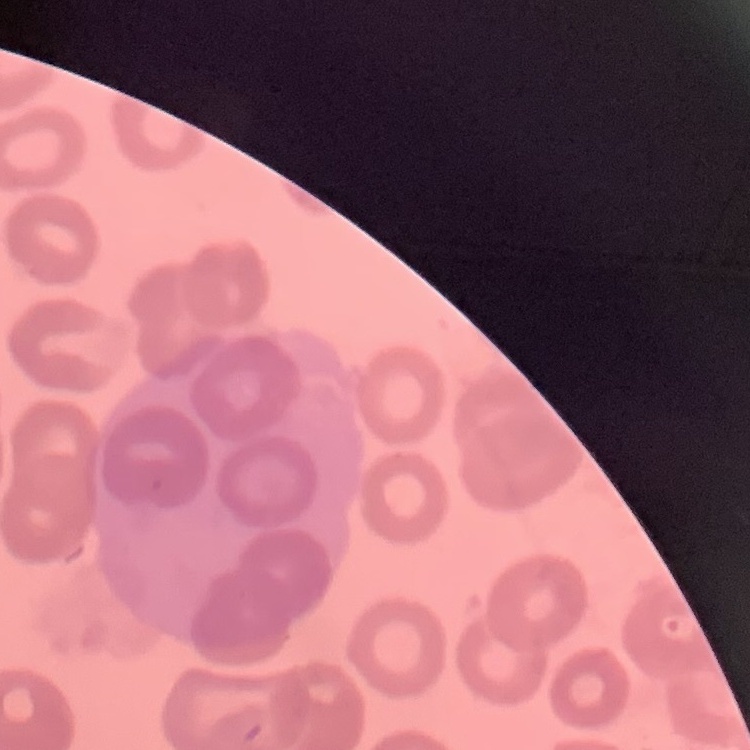
The erythrocytes exhibit no rouleaux formation. Stained with either Field's or Giemsa. Thin peripheral smear. Square crop of a larger photomicrograph.